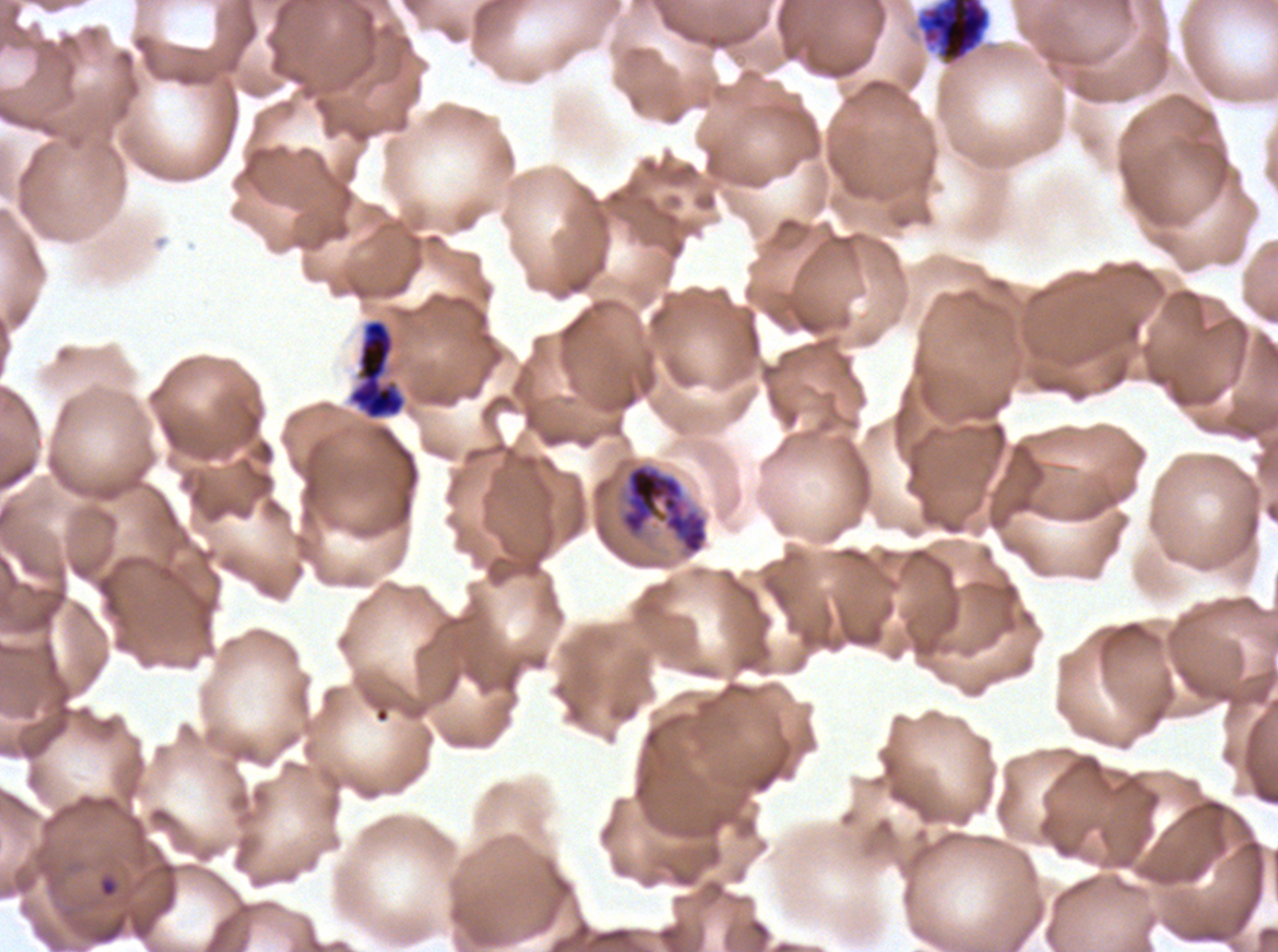
Approximate bounding boxes as {x1, y1, x2, y2} in pixels. Early schizont locations: {915, 0, 991, 65}, {347, 318, 407, 421}, {620, 462, 708, 555}. Ring locations: {98, 875, 118, 898}. Thin blood smear. Life-cycle stages observed: ring, early schizont. One sub-image of a larger composite. Ex-vivo P. falciparum culture from a patient in The Gambia, grown for 24 to 48 hours. Giemsa stain. Image is 1278×952 pixels.